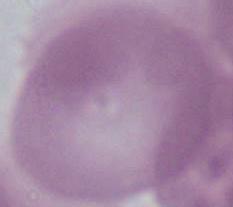
Summary:
  - Identification: red blood cell
  - Modality: micrograph
  - Magnification: 1000x